Name the blood parasite species.
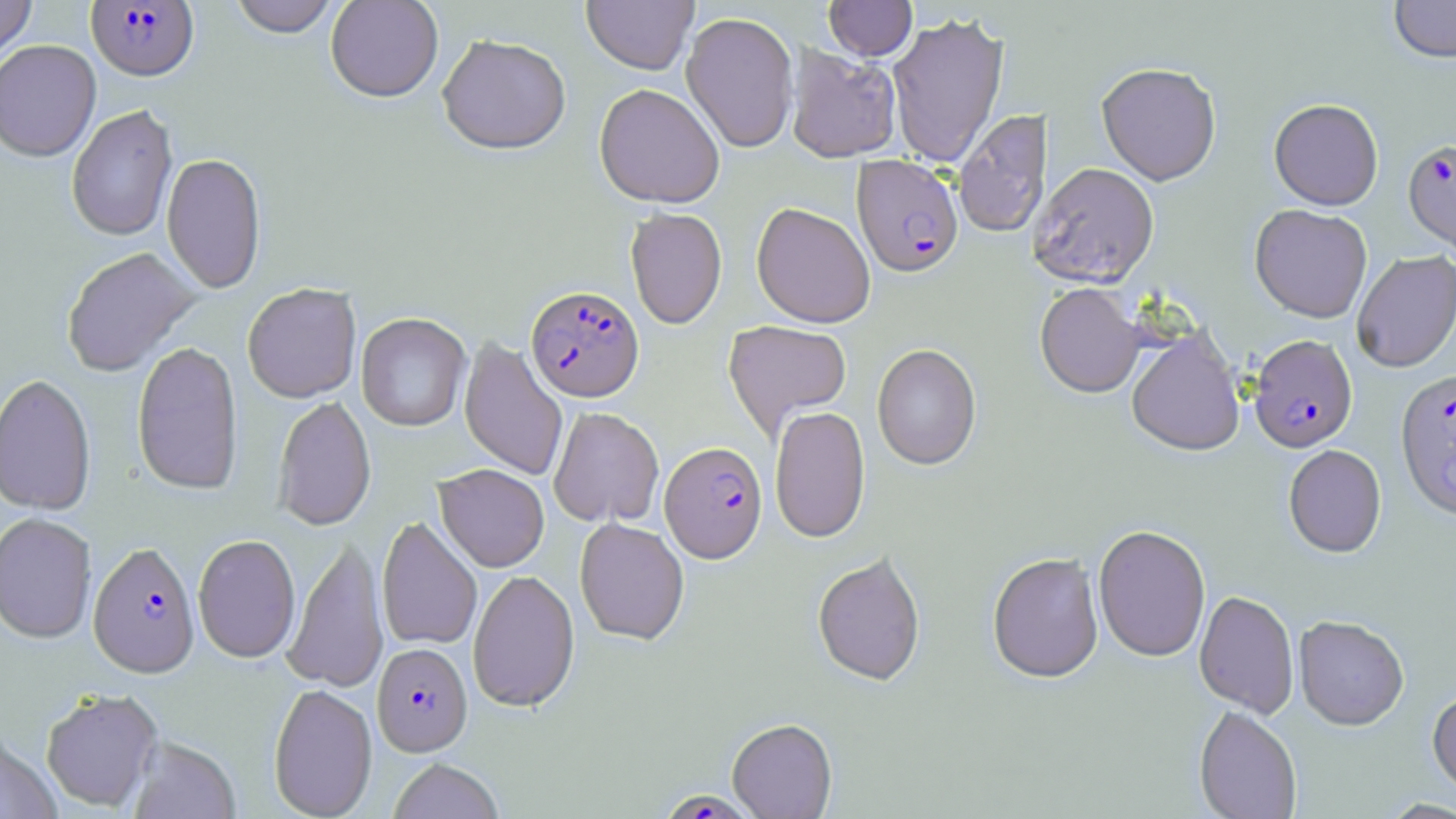
Plasmodium falciparum.

{
  "uninfected_red_blood_cell_locations": "approximate bounding boxes as [x1, y1, x2, y2] in pixels: [0, 0, 37, 64], [229, 0, 341, 40], [326, 0, 444, 106], [581, 0, 699, 78], [823, 0, 917, 64], [1389, 0, 1456, 66], [681, 15, 798, 154], [887, 16, 1010, 168], [437, 38, 572, 159], [0, 42, 101, 165], [785, 46, 901, 164], [1096, 66, 1221, 189], [594, 85, 725, 211], [1268, 102, 1383, 214], [67, 106, 178, 243], [954, 111, 1053, 240], [161, 155, 266, 295], [1027, 166, 1159, 292], [751, 205, 875, 330], [1249, 207, 1371, 325], [626, 208, 728, 331], [61, 249, 201, 378], [1352, 252, 1456, 374], [242, 284, 362, 404], [1035, 286, 1145, 400], [355, 313, 471, 433], [723, 321, 851, 440], [1126, 331, 1245, 459], [459, 337, 568, 481], [132, 343, 244, 497], [871, 346, 982, 472], [0, 374, 97, 516], [272, 396, 376, 532], [770, 407, 871, 545], [548, 408, 664, 528], [1283, 447, 1387, 560], [434, 464, 549, 573], [0, 512, 96, 645], [377, 517, 482, 651], [574, 519, 689, 647], [1093, 527, 1210, 665], [193, 535, 301, 664], [283, 539, 389, 694], [812, 556, 927, 689], [987, 556, 1104, 686], [468, 571, 580, 714], [1194, 592, 1299, 720], [1294, 617, 1409, 734], [268, 683, 378, 819], [40, 689, 164, 812], [1427, 689, 1456, 799], [1193, 708, 1302, 819], [727, 720, 838, 819], [0, 733, 62, 819], [128, 737, 241, 818], [388, 760, 505, 819], [1379, 798, 1456, 818]",
  "stain": "May-Grünwald-Giemsa",
  "magnification": "1000x",
  "plasmodium_falciparum_infected_red_blood_cell_locations": "approximate bounding boxes as [x1, y1, x2, y2] in pixels: [86, 1, 200, 84], [1403, 141, 1456, 260], [852, 157, 963, 280], [525, 287, 645, 405], [1249, 337, 1358, 456], [1395, 372, 1456, 526], [659, 443, 768, 565], [87, 542, 200, 679], [372, 643, 472, 758], [657, 789, 760, 818]",
  "image_size": "1456×819 pixels",
  "preparation": "thin blood smear",
  "modality": "light microscopy",
  "field_of_view": "one of a larger specimen"
}